State the preparation type.
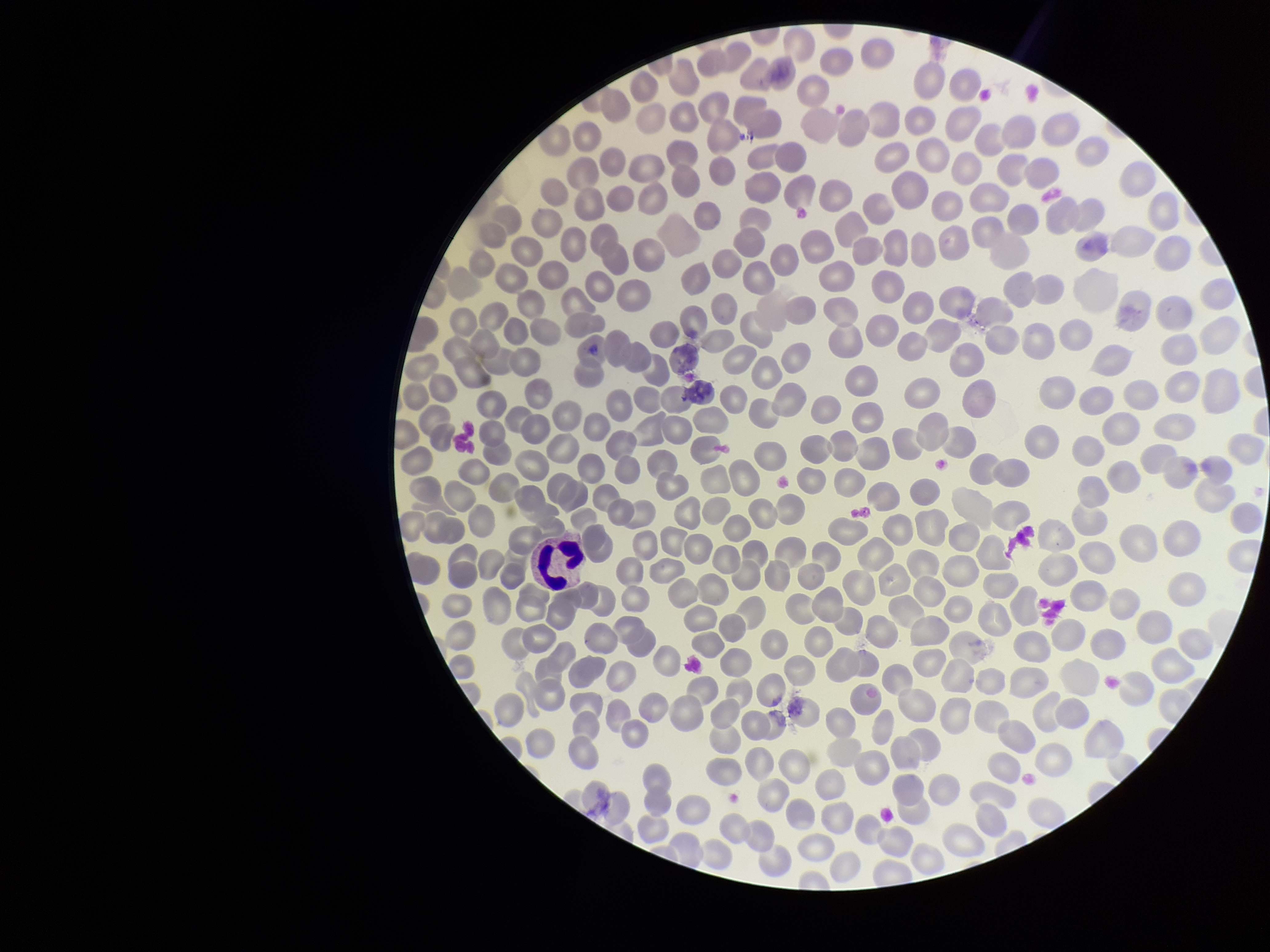
Thin.

Summary:
  - Patient malaria status: negative
  - Capture: smartphone photograph through the microscope eyepiece
  - Parasitized red blood cells: none detected
  - Image size: 1270×952 pixels
  - Parasitized red blood cell count: 0
  - Stain: Giemsa
  - Red blood cell count: 281
  - Field of view: one from this slide